Classify this cell by malaria status.
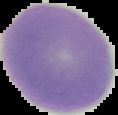

It is uninfected.

Summary:
  - Image size: 118×115 pixels
  - Image type: cell region segmented out of the field of view; surrounding area masked to black
  - Preparation: thin blood smear